Outline each blood parasite and name the species.
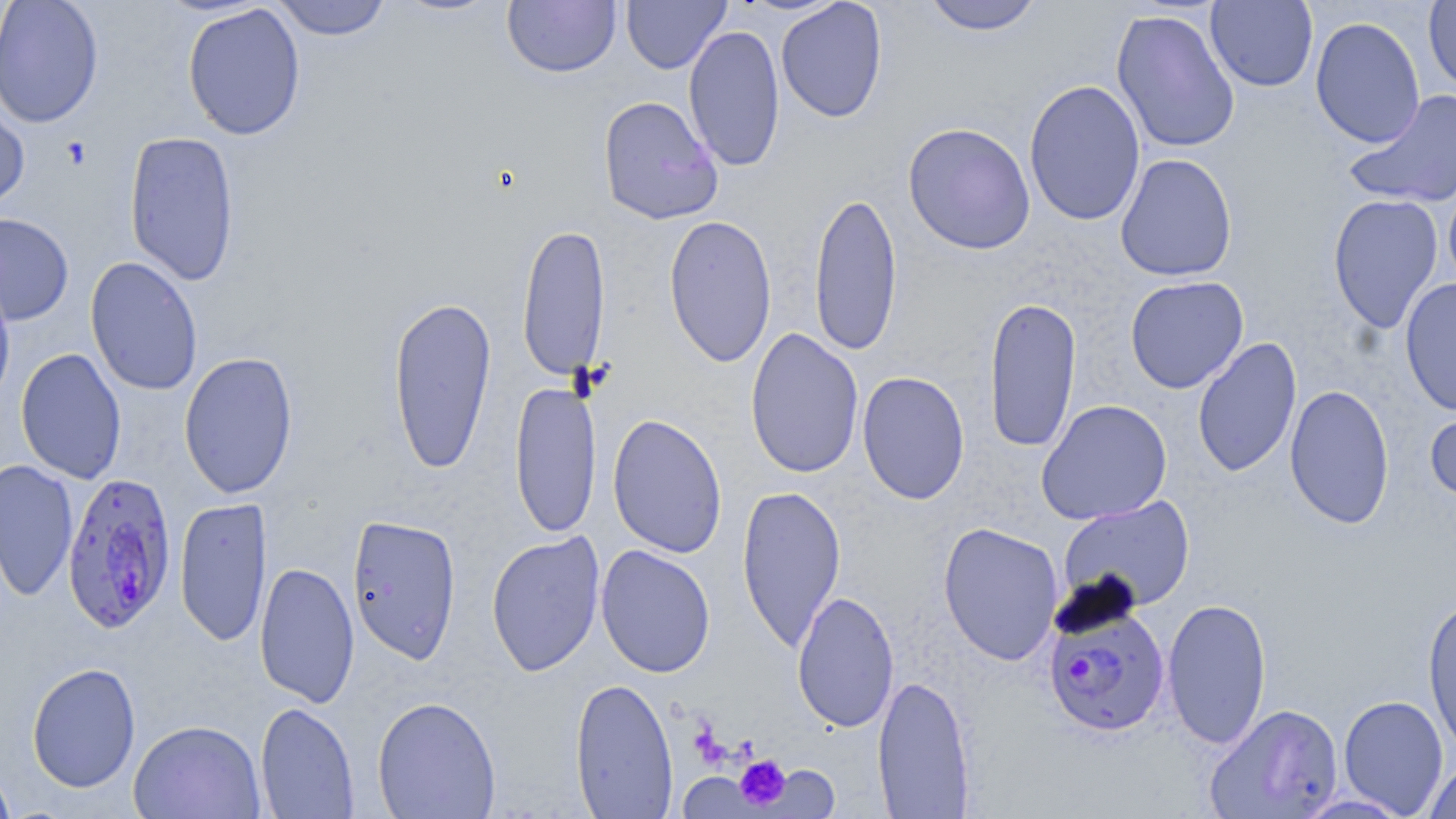
Approximate bounding boxes as [x1, y1, x2, y2] in pixels.
Plasmodium falciparum-infected red blood cells: [61, 470, 177, 634], [1043, 601, 1171, 736].
No Plasmodium ovale, Plasmodium malariae, Plasmodium vivax, Babesia divergens, or Trypanosoma brucei observed.

slide-level diagnosis = Plasmodium falciparum
platelet locations = approximate bounding boxes as [x1, y1, x2, y2] in pixels: [61, 137, 92, 170], [735, 755, 791, 810]
preparation = thin blood film
field of view = single
modality = light microscopy
image size = 1456×819 pixels
stain = May-Grünwald-Giemsa
magnification = 1000x
uninfected red blood cell locations = approximate bounding boxes as [x1, y1, x2, y2] in pixels: [0, 0, 104, 129], [270, 0, 393, 41], [390, 0, 506, 17], [621, 0, 730, 74], [922, 0, 1044, 36], [502, 1, 620, 78], [775, 1, 888, 123], [1205, 1, 1318, 92], [1423, 1, 1456, 95], [182, 3, 306, 141], [1111, 8, 1240, 154], [1310, 16, 1425, 148], [683, 23, 785, 173], [1024, 78, 1145, 226], [1344, 90, 1456, 210], [0, 91, 30, 214], [597, 95, 723, 225], [902, 122, 1036, 255], [124, 130, 241, 287], [1115, 154, 1238, 282], [1443, 177, 1456, 296], [809, 190, 902, 358], [1328, 193, 1443, 335], [0, 213, 74, 325], [664, 215, 777, 368], [516, 222, 611, 383], [85, 256, 204, 396], [0, 273, 15, 408], [1125, 276, 1248, 394], [1400, 277, 1456, 417], [387, 294, 497, 475], [984, 295, 1081, 454], [745, 329, 864, 478], [1192, 337, 1302, 478], [15, 347, 127, 484], [178, 351, 299, 500], [857, 371, 970, 505], [510, 379, 602, 540], [1284, 384, 1395, 530], [1036, 399, 1172, 524], [1424, 400, 1456, 508], [607, 413, 727, 558], [0, 459, 78, 602], [736, 484, 846, 652], [1058, 495, 1195, 614], [175, 496, 272, 648], [347, 514, 461, 664], [938, 521, 1063, 666], [486, 530, 606, 678], [595, 544, 716, 679], [254, 560, 360, 708], [792, 590, 899, 733], [1422, 595, 1456, 755], [1161, 597, 1272, 749], [26, 661, 141, 793], [872, 673, 975, 818], [570, 677, 678, 818], [1338, 694, 1449, 817], [372, 696, 501, 818], [255, 701, 360, 819], [1204, 703, 1344, 818], [129, 719, 266, 819], [1423, 759, 1456, 819], [0, 764, 18, 818], [759, 764, 840, 817], [678, 771, 764, 817], [1292, 792, 1414, 819]